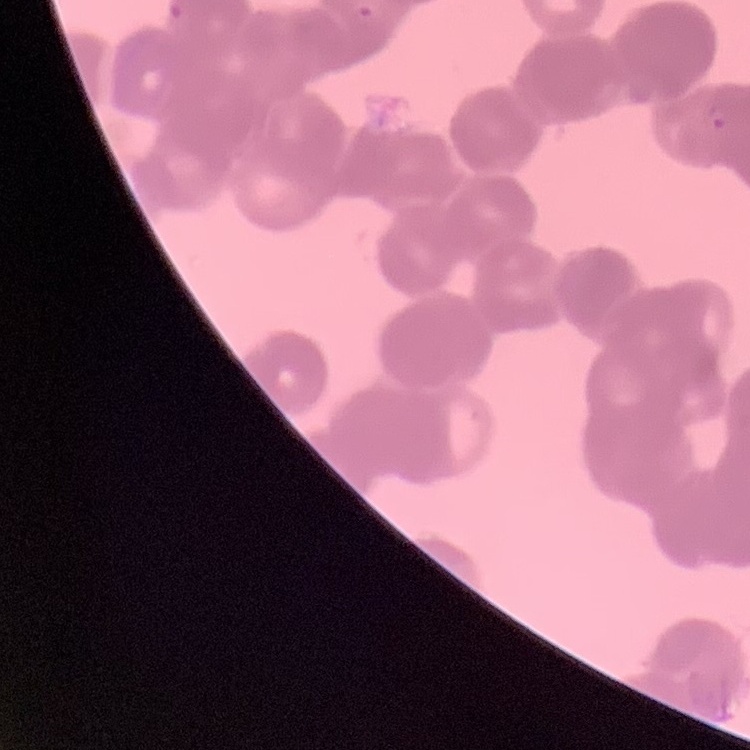

erythrocyte morphology = rouleaux formation
preparation = thin blood film
image type = one tile cut from a larger photomicrograph
stain = Field's or Giemsa